Outline every leukocyte.
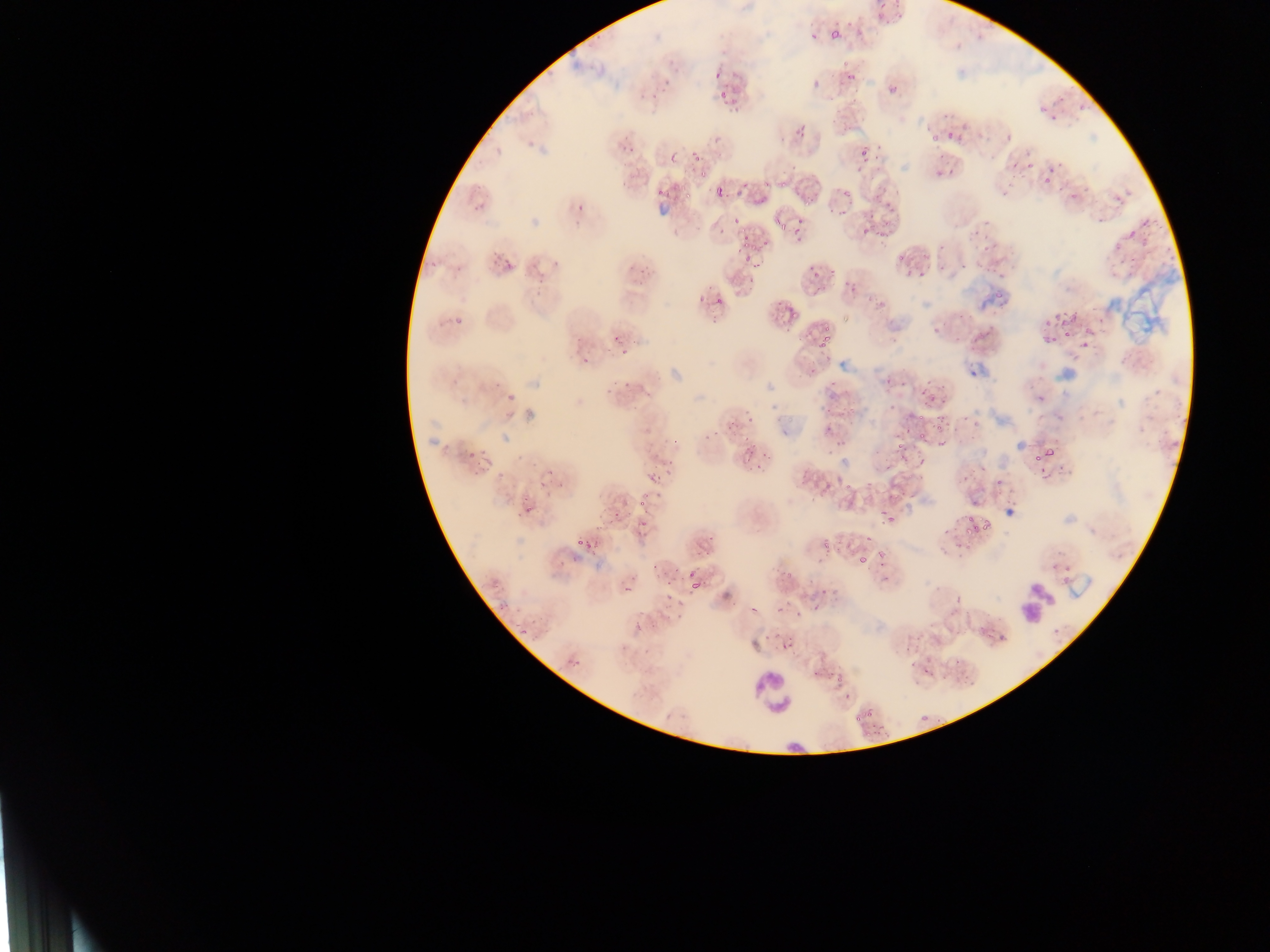
Approximate bounding boxes as (left, top, right, bottom) in pixels.
Leukocytes: (751, 669, 797, 721).

{
  "capture": "mobile-phone photograph through a microscope",
  "malaria_parasite_locations": "approximate bounding boxes as (left, top, right, bottom) in pixels: (822, 30, 839, 46), (646, 63, 674, 108), (840, 65, 860, 88), (713, 71, 722, 81), (890, 85, 898, 92), (939, 123, 969, 150), (616, 136, 639, 156), (851, 140, 876, 157), (690, 147, 700, 164), (1006, 152, 1032, 176), (665, 154, 682, 167), (1041, 168, 1060, 187), (704, 171, 736, 206), (828, 181, 853, 216), (657, 188, 667, 197), (874, 189, 897, 230), (576, 204, 585, 213), (787, 217, 808, 233), (858, 218, 877, 238), (730, 237, 750, 264), (750, 255, 769, 276), (896, 257, 922, 280), (803, 262, 820, 282), (714, 294, 724, 306), (1041, 301, 1082, 351), (772, 302, 798, 322), (803, 321, 814, 347), (816, 323, 839, 365), (612, 330, 620, 344), (965, 332, 984, 357), (614, 343, 632, 360), (581, 357, 590, 366), (606, 376, 638, 404), (921, 382, 945, 410), (820, 387, 843, 419), (507, 393, 517, 403), (715, 412, 740, 438), (913, 413, 954, 448), (461, 438, 478, 476), (740, 440, 758, 460), (1041, 443, 1062, 457), (749, 450, 769, 473), (1034, 452, 1043, 461), (666, 461, 687, 506), (539, 470, 556, 490), (644, 472, 664, 488), (815, 479, 841, 500), (627, 498, 647, 524), (880, 499, 907, 525), (518, 506, 544, 522), (964, 508, 991, 545), (818, 531, 836, 560), (577, 533, 597, 562), (854, 547, 875, 579), (701, 554, 721, 565), (679, 563, 700, 583), (766, 564, 789, 587), (652, 565, 674, 583), (611, 576, 639, 592), (687, 579, 704, 598), (795, 586, 818, 609), (662, 588, 683, 624), (778, 610, 789, 619), (514, 615, 537, 644), (773, 633, 799, 660), (833, 655, 848, 691), (809, 658, 822, 683), (909, 662, 934, 683), (958, 666, 975, 681), (850, 713, 871, 729)",
  "country": "Ghana",
  "preparation": "thin blood film",
  "field_of_view": "single",
  "image_size": "1270×952 pixels"
}